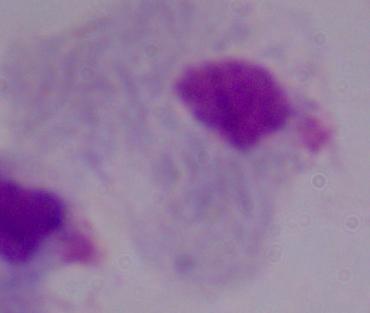

{
  "modality": "photomicrograph",
  "identification": "trichomonad",
  "magnification": "1000x"
}